Report the malaria status.
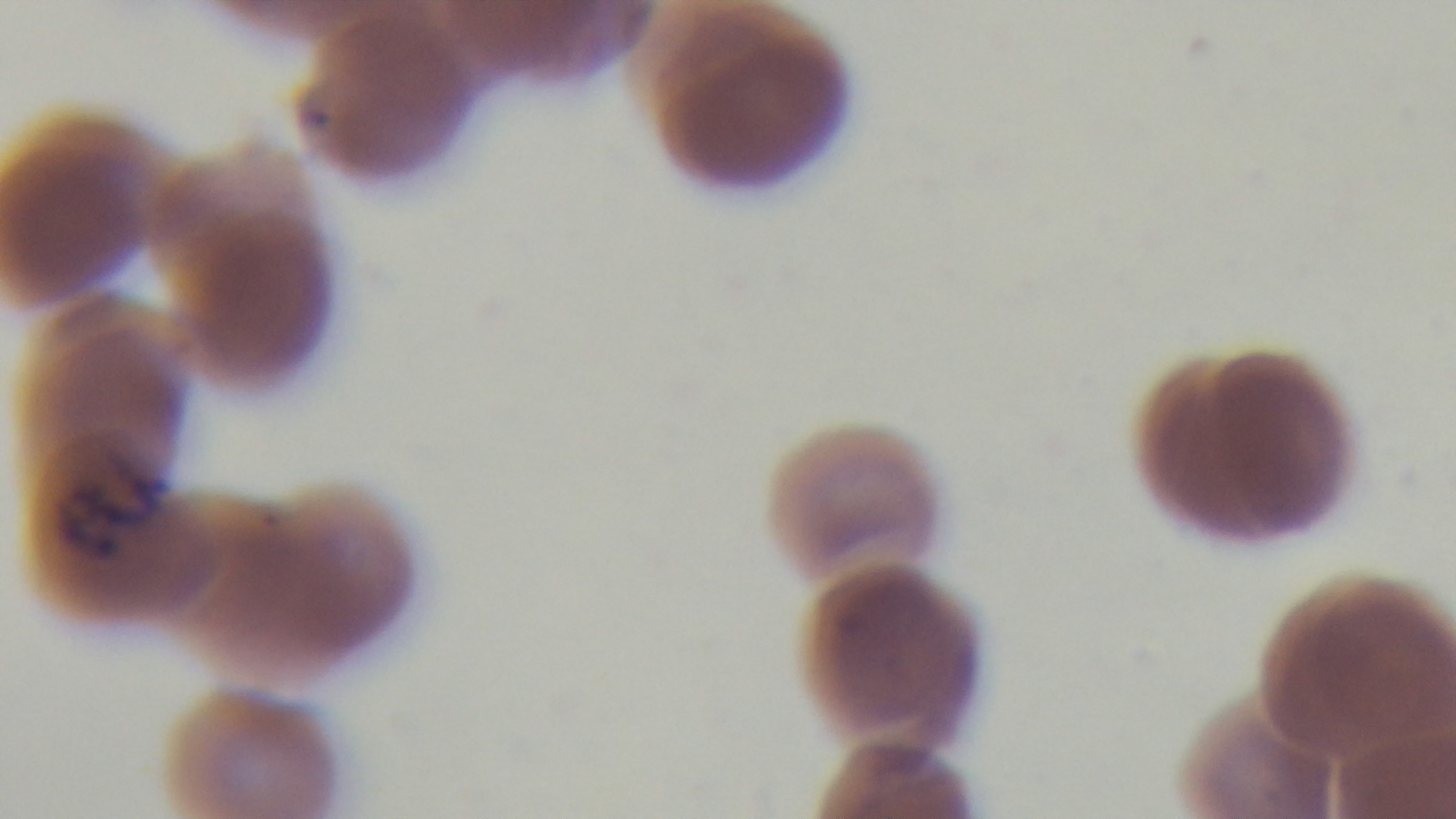

Infected.

stain: Giemsa
capture: mounted 4K digital camera
modality: light microscopy
objective: 100x oil immersion
preparation: thin smear
field_of_view: one from the slide